Report the malaria status of this cell.
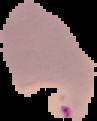

Parasitized.

{
  "preparation": "thin blood film",
  "image_type": "segmented cell region on a black background",
  "image_size": "97×121 pixels"
}